Report the malaria status of this cell.
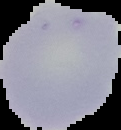
It is uninfected.

image size = 121×130 pixels
image type = segmented cell region on a black background
preparation = thin blood film